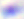
Summary:
  - Magnification: 400x
  - Modality: photomicrograph
  - Identification: Toxoplasma gondii